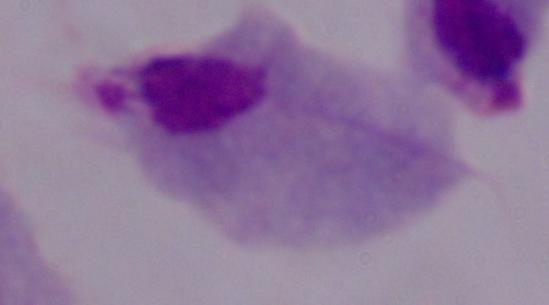

magnification = 1000x
identification = trichomonad
modality = micrograph